Report the malaria status of this cell.
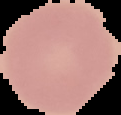

Uninfected.

Summary:
  - Preparation: thin blood film
  - Image size: 121×115 pixels
  - Image type: cell region segmented out of the field of view; surrounding area masked to black